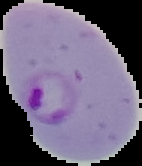
image type = cell region segmented out of the field of view; surrounding area masked to black
image size = 142×166 pixels
preparation = thin blood film
result = malaria parasites detected